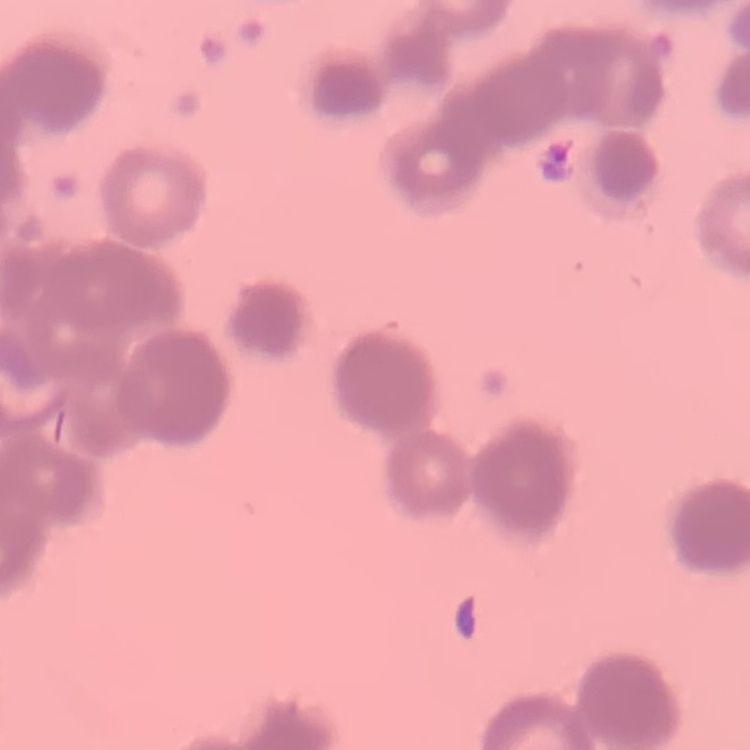

erythrocyte morphology = rouleaux formation
stain = Field's or Giemsa
preparation = thin blood smear
image type = square crop of a larger photomicrograph